Outline each uninfected red blood cell.
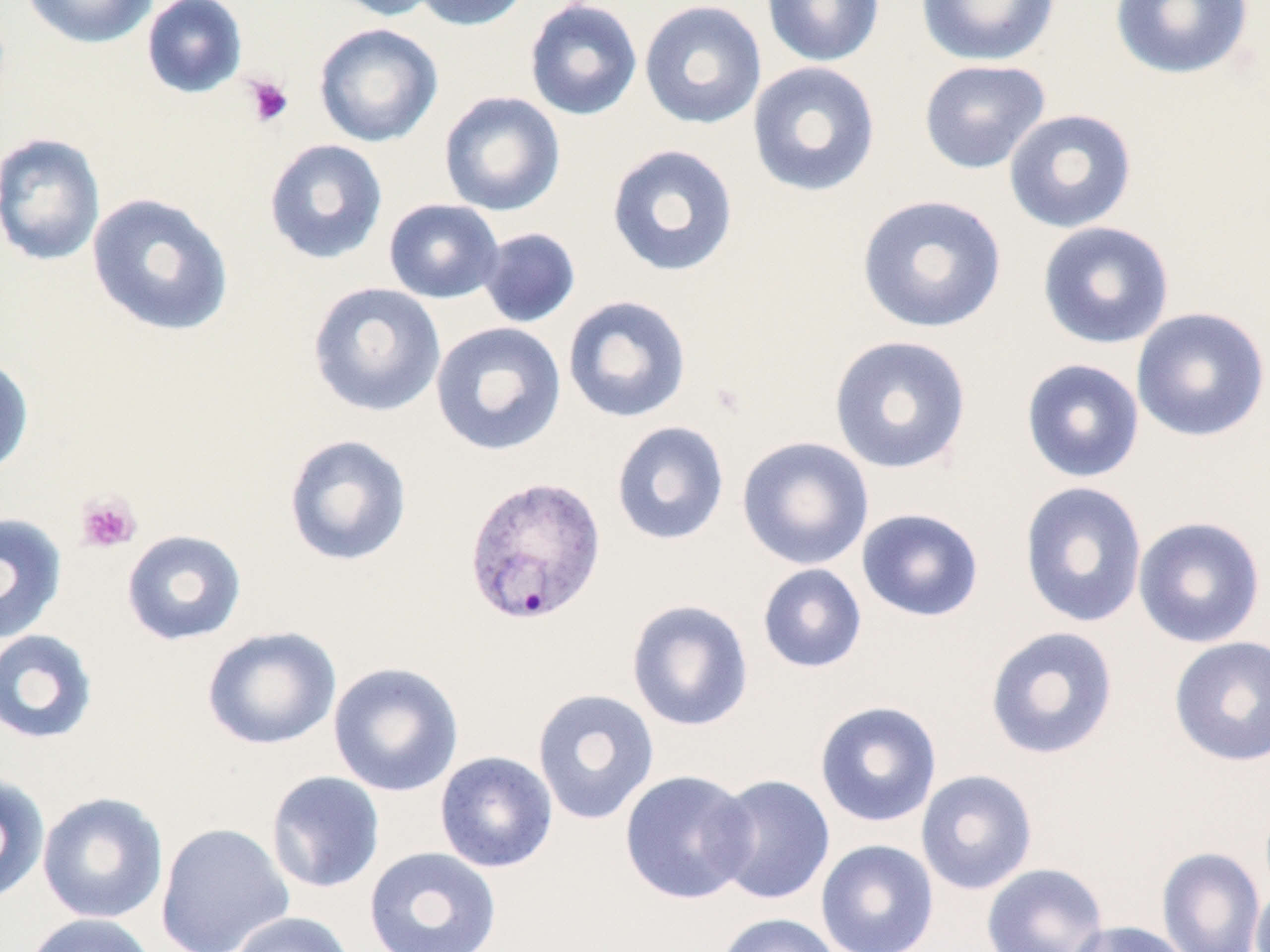

Approximate bounding boxes as (x1, y1, x2, y2) in pixels.
Uninfected red blood cells: (21, 0, 158, 49), (142, 0, 248, 99), (325, 0, 446, 21), (410, 0, 534, 32), (523, 0, 643, 121), (638, 0, 767, 130), (761, 0, 884, 67), (915, 0, 1061, 67), (1109, 0, 1254, 81), (313, 22, 443, 147), (918, 59, 1051, 175), (746, 61, 881, 198), (438, 91, 566, 217), (1002, 108, 1138, 233), (0, 132, 106, 267), (263, 138, 388, 266), (606, 143, 739, 278), (86, 192, 235, 337), (855, 194, 1008, 334), (383, 198, 504, 304), (1036, 221, 1175, 349), (478, 227, 581, 329), (307, 281, 446, 417), (561, 295, 692, 424), (1130, 306, 1270, 443), (430, 321, 567, 457), (828, 334, 973, 475), (0, 354, 34, 478), (1020, 358, 1145, 483), (610, 420, 730, 546), (282, 433, 413, 568), (736, 436, 874, 571), (1018, 481, 1149, 629), (856, 507, 985, 623), (0, 513, 68, 643), (1132, 516, 1267, 648), (121, 529, 247, 646), (757, 563, 867, 674), (626, 598, 754, 732), (201, 625, 342, 751), (984, 626, 1119, 761), (0, 628, 99, 745), (1167, 635, 1270, 767), (328, 661, 464, 797), (531, 688, 660, 825), (813, 700, 943, 827), (434, 750, 558, 873), (619, 769, 757, 904), (915, 769, 1038, 895), (265, 771, 385, 894), (0, 773, 51, 905), (708, 773, 836, 906), (37, 791, 169, 924), (155, 821, 294, 952), (815, 839, 939, 952), (364, 846, 502, 952), (1156, 847, 1266, 952), (981, 863, 1109, 952), (1251, 882, 1270, 952), (226, 911, 358, 952), (715, 912, 843, 952), (22, 913, 161, 952), (1066, 920, 1194, 952).

slide-level diagnosis = Plasmodium vivax
preparation = thin blood smear
platelet locations = approximate bounding boxes as (x1, y1, x2, y2) in pixels: (243, 74, 295, 128), (75, 492, 141, 554)
magnification = 1000x
stain = May-Grünwald-Giemsa
modality = optical microscopy
image size = 1270×952 pixels
field of view = one of a larger specimen
Plasmodium vivax-infected red blood cell locations = approximate bounding boxes as (x1, y1, x2, y2) in pixels: (462, 473, 607, 625)